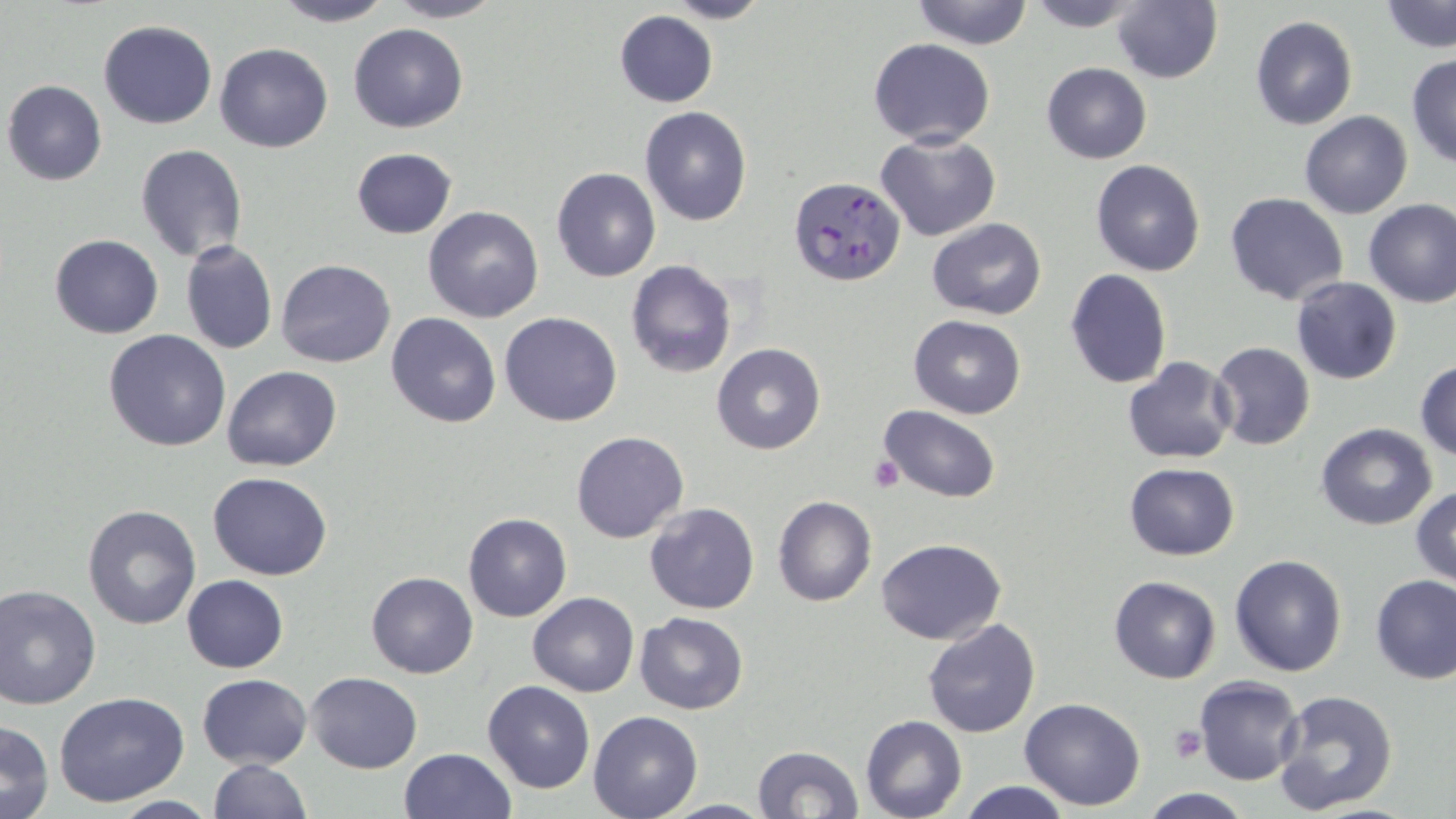 Approximate bounding boxes as named x1/y1/x2/y2 corners in pixels. Platelet locations: (x1=868, y1=456, x2=905, y2=493), (x1=1169, y1=727, x2=1205, y2=764). Plasmodium falciparum-infected red blood cell locations: (x1=788, y1=177, x2=905, y2=287). Uninfected red blood cell locations: (x1=271, y1=0, x2=396, y2=27), (x1=385, y1=0, x2=506, y2=23), (x1=659, y1=0, x2=770, y2=25), (x1=910, y1=0, x2=1035, y2=50), (x1=1024, y1=0, x2=1148, y2=29), (x1=1112, y1=0, x2=1223, y2=85), (x1=1381, y1=1, x2=1456, y2=53), (x1=613, y1=11, x2=719, y2=107), (x1=1248, y1=15, x2=1358, y2=130), (x1=99, y1=19, x2=216, y2=129), (x1=349, y1=23, x2=468, y2=132), (x1=868, y1=38, x2=995, y2=148), (x1=214, y1=42, x2=333, y2=153), (x1=1406, y1=53, x2=1456, y2=167), (x1=1041, y1=62, x2=1152, y2=164), (x1=3, y1=80, x2=108, y2=185), (x1=639, y1=105, x2=752, y2=227), (x1=1299, y1=110, x2=1412, y2=219), (x1=876, y1=132, x2=1000, y2=240), (x1=134, y1=144, x2=248, y2=264), (x1=351, y1=148, x2=456, y2=240), (x1=1090, y1=159, x2=1207, y2=276), (x1=551, y1=167, x2=660, y2=282), (x1=1225, y1=193, x2=1349, y2=306), (x1=1363, y1=198, x2=1456, y2=307), (x1=423, y1=207, x2=545, y2=324), (x1=927, y1=217, x2=1047, y2=321), (x1=49, y1=234, x2=163, y2=339), (x1=180, y1=241, x2=277, y2=355), (x1=276, y1=258, x2=396, y2=368), (x1=626, y1=260, x2=737, y2=380), (x1=1064, y1=268, x2=1173, y2=390), (x1=1290, y1=276, x2=1402, y2=385), (x1=386, y1=312, x2=501, y2=428), (x1=498, y1=312, x2=621, y2=427), (x1=908, y1=315, x2=1027, y2=419), (x1=103, y1=329, x2=231, y2=452), (x1=1209, y1=342, x2=1315, y2=451), (x1=712, y1=343, x2=825, y2=455), (x1=1123, y1=356, x2=1238, y2=464), (x1=1415, y1=359, x2=1456, y2=461), (x1=222, y1=365, x2=342, y2=471), (x1=877, y1=405, x2=1002, y2=504), (x1=1316, y1=423, x2=1436, y2=531), (x1=572, y1=431, x2=688, y2=543), (x1=1123, y1=463, x2=1240, y2=561), (x1=208, y1=471, x2=332, y2=580), (x1=1411, y1=485, x2=1456, y2=588), (x1=773, y1=496, x2=877, y2=607), (x1=643, y1=502, x2=761, y2=615), (x1=81, y1=504, x2=201, y2=631), (x1=463, y1=513, x2=572, y2=623), (x1=876, y1=538, x2=1005, y2=644), (x1=1230, y1=554, x2=1347, y2=677), (x1=366, y1=571, x2=478, y2=677), (x1=181, y1=574, x2=289, y2=673), (x1=1108, y1=575, x2=1221, y2=684), (x1=1372, y1=576, x2=1456, y2=685), (x1=0, y1=583, x2=101, y2=709), (x1=528, y1=592, x2=639, y2=696), (x1=635, y1=612, x2=749, y2=713), (x1=921, y1=618, x2=1039, y2=739), (x1=305, y1=672, x2=422, y2=773), (x1=197, y1=673, x2=311, y2=768), (x1=1195, y1=677, x2=1303, y2=785), (x1=482, y1=680, x2=596, y2=795), (x1=1272, y1=688, x2=1398, y2=813), (x1=55, y1=693, x2=188, y2=807), (x1=1019, y1=697, x2=1146, y2=810), (x1=588, y1=710, x2=702, y2=819), (x1=860, y1=715, x2=967, y2=819), (x1=0, y1=719, x2=55, y2=819), (x1=752, y1=744, x2=864, y2=819), (x1=398, y1=748, x2=516, y2=818), (x1=208, y1=759, x2=310, y2=819), (x1=955, y1=779, x2=1076, y2=819), (x1=1138, y1=790, x2=1257, y2=819), (x1=104, y1=796, x2=220, y2=818). Slide-level diagnosis: Plasmodium falciparum. May-Grünwald-Giemsa-stained preparation. One field of a larger specimen. Thin blood smear. Optical microscopy. Captured at 1000x magnification. Image is 1456×819 pixels.